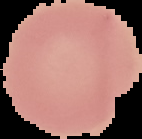
Summary:
  - Preparation: thin blood film
  - Result: no malaria parasites detected
  - Image type: segmented cell region on a black background
  - Image size: 142×139 pixels